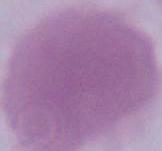
Summary:
  - Modality: photomicrograph
  - Magnification: 1000x
  - Identification: erythrocyte